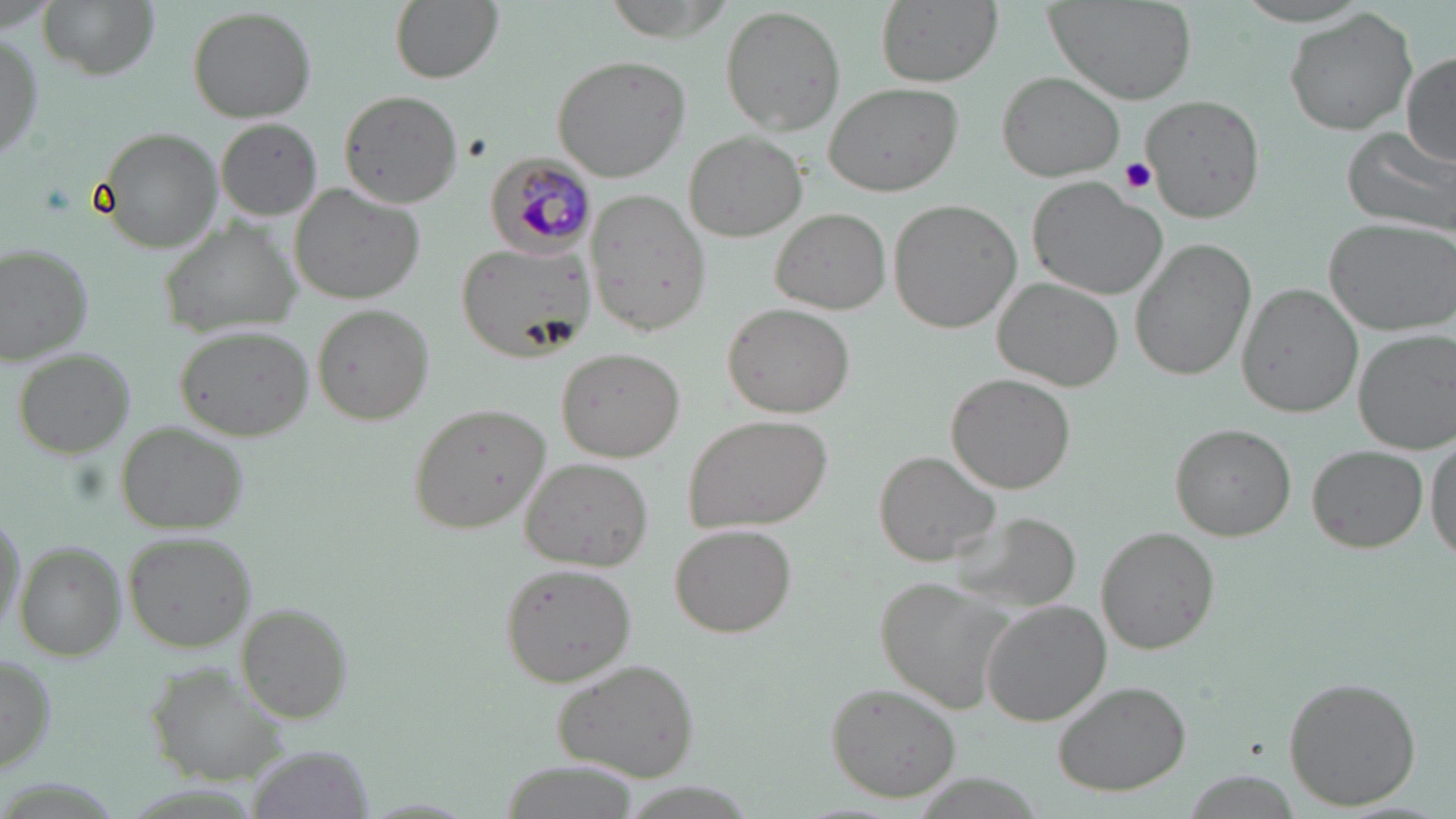
Summary:
  - Coordinate format: approximate bounding boxes as (x1,y1)-(x2,y2) corner pairs in pixels
  - Plasmodium malariae-infected red blood cell locations: (483,152)-(597,255)
  - Platelet locations: (1117,158)-(1156,197)
  - Uninfected red blood cell locations: (37,0)-(157,80), (387,0)-(503,82), (601,0)-(733,41), (873,0)-(1003,87), (1045,0)-(1196,104), (1227,1)-(1380,29), (720,4)-(845,137), (188,5)-(319,120), (1283,9)-(1419,136), (0,28)-(44,168), (551,53)-(691,182), (1400,54)-(1456,166), (997,71)-(1125,181), (824,82)-(962,198), (339,89)-(463,207), (1141,97)-(1266,223), (216,118)-(323,220), (96,126)-(222,251), (1342,127)-(1456,238), (684,131)-(806,241), (1029,177)-(1168,299), (289,181)-(428,303), (586,190)-(709,334), (891,199)-(1024,333), (770,206)-(890,314), (1323,216)-(1455,334), (157,220)-(300,336), (454,239)-(591,363), (1130,239)-(1255,380), (1,244)-(95,366), (993,277)-(1122,391), (1238,283)-(1359,416), (312,303)-(434,427), (724,304)-(852,419), (175,323)-(312,440), (1353,327)-(1455,453), (13,346)-(135,458), (556,347)-(684,462), (946,374)-(1074,494), (407,401)-(551,534), (681,413)-(833,533), (116,421)-(248,535), (1170,422)-(1296,542), (1427,431)-(1456,566), (1309,445)-(1427,552), (875,450)-(998,564), (519,455)-(654,570), (0,507)-(25,637), (954,511)-(1081,615), (670,523)-(797,639), (1097,527)-(1218,653), (124,532)-(257,653), (15,542)-(127,659), (499,563)-(635,687), (876,576)-(1024,716), (982,599)-(1112,725), (236,603)-(354,725), (0,651)-(55,777), (549,658)-(702,782), (145,666)-(294,786), (1281,675)-(1422,812), (1050,678)-(1192,796), (824,683)-(962,801), (252,743)-(374,818), (498,759)-(637,818)
  - Slide-level diagnosis: Plasmodium malariae
  - Modality: light microscopy
  - Field of view: one of a larger specimen
  - Stain: May-Grünwald-Giemsa
  - Preparation: thin blood film
  - Image size: 1456×819 pixels
  - Magnification: 1000x